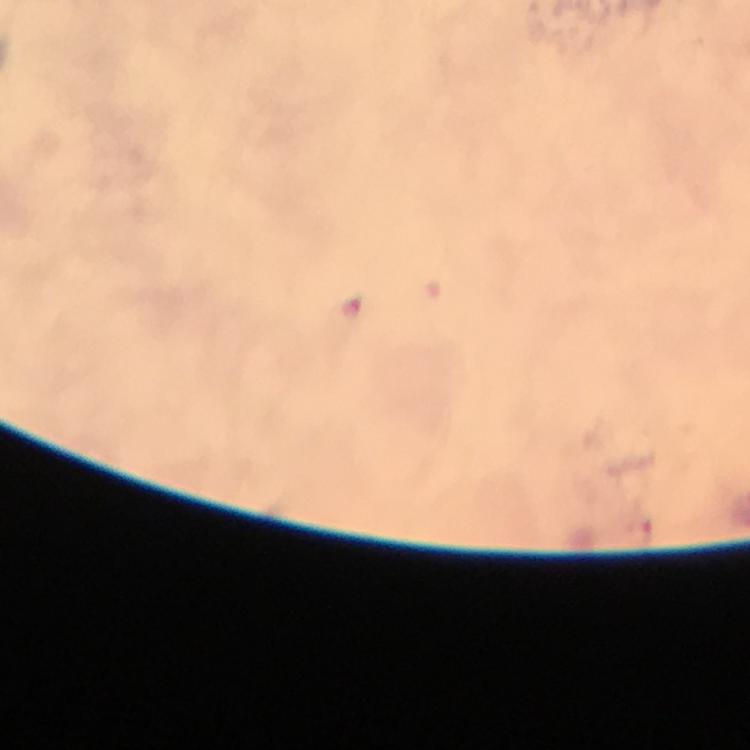

Approximate centers as {x, y} in pixels. Malaria parasite locations: {353, 308}, {638, 530}. Thick blood film. At 100x magnification. Immersion oil was used. Cropped region of a single field of view. Photographed with a smartphone mounted on the microscope. Image is 750×750 pixels. Giemsa stain. From a diagnostic examination for malaria.